State the preparation type.
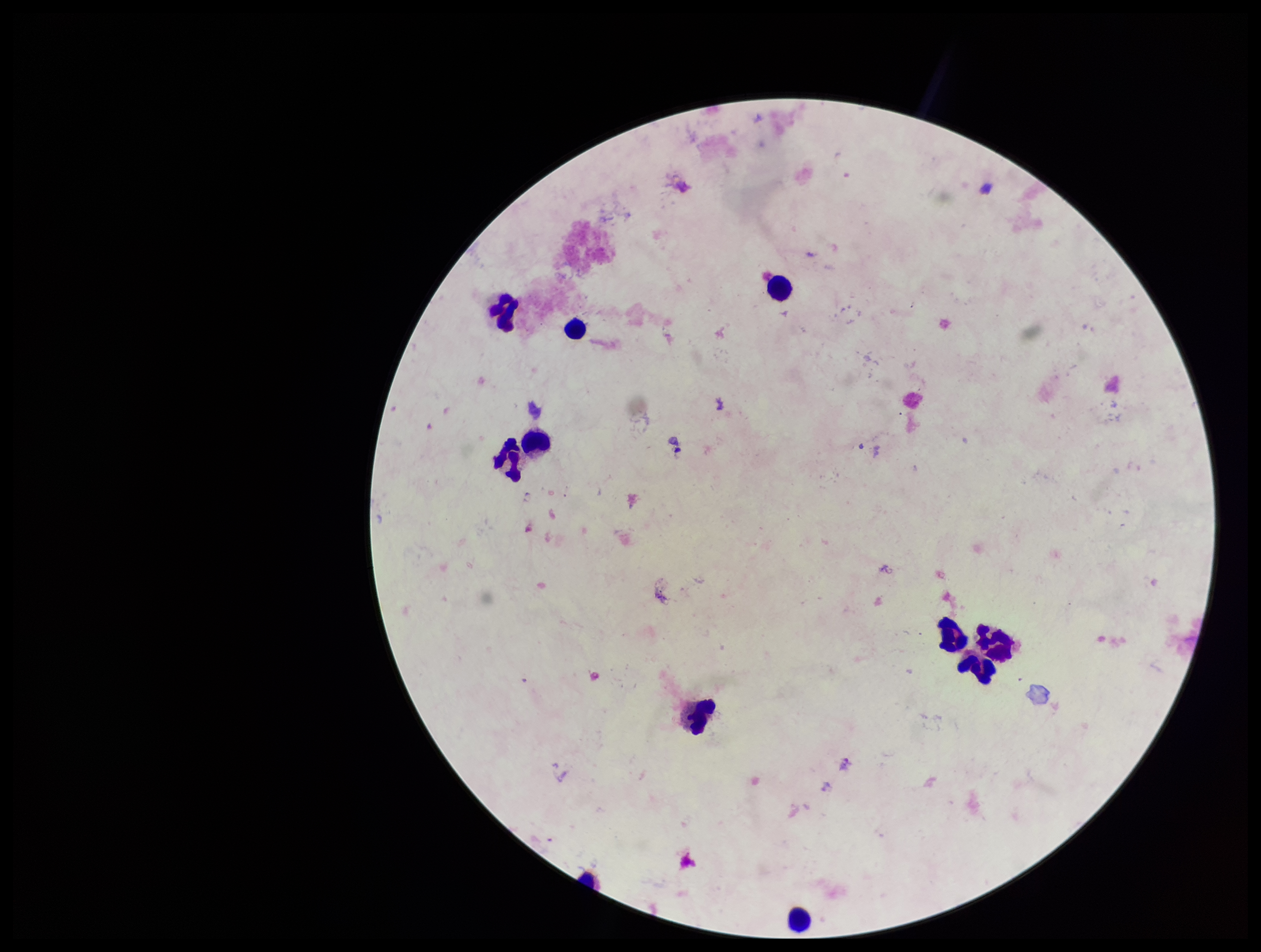
A thick smear.

Plasmodium parasites: none identified. Patient malaria status: negative. Image is 1261×952 pixels. Smartphone photograph taken through the eyepiece of a microscope. One field from this slide. Leukocyte count: 10. Stained with Giemsa. Parasite count: 0.